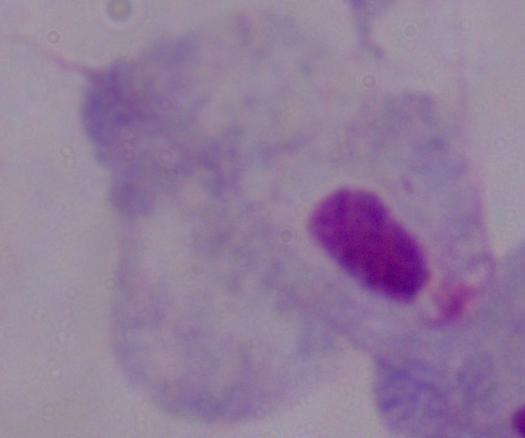
identification: trichomonad
modality: photomicrograph
magnification: 1000x